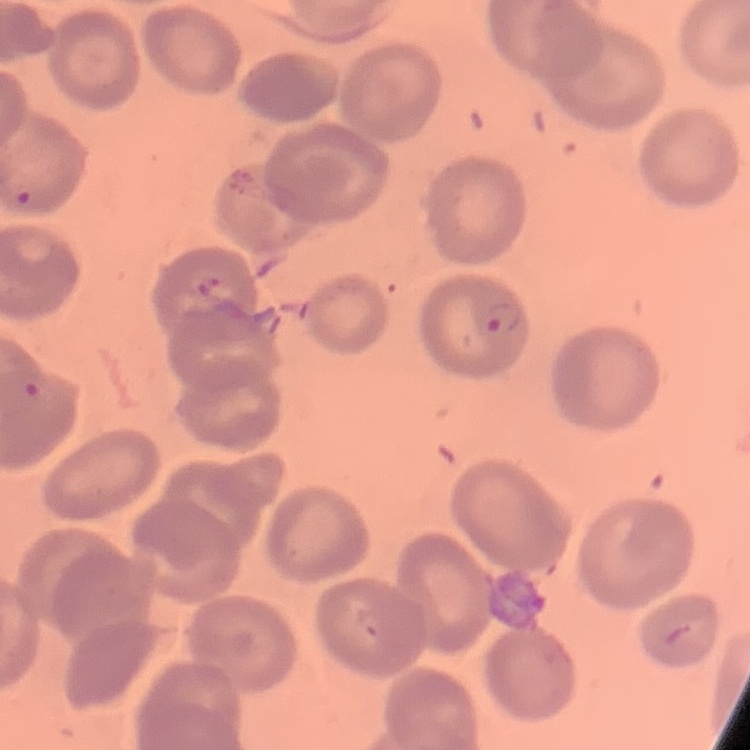

red_blood_cell_morphology: no rouleaux formation
stain: Field's or Giemsa
image_type: one tile cut from a larger photomicrograph
preparation: thin blood smear